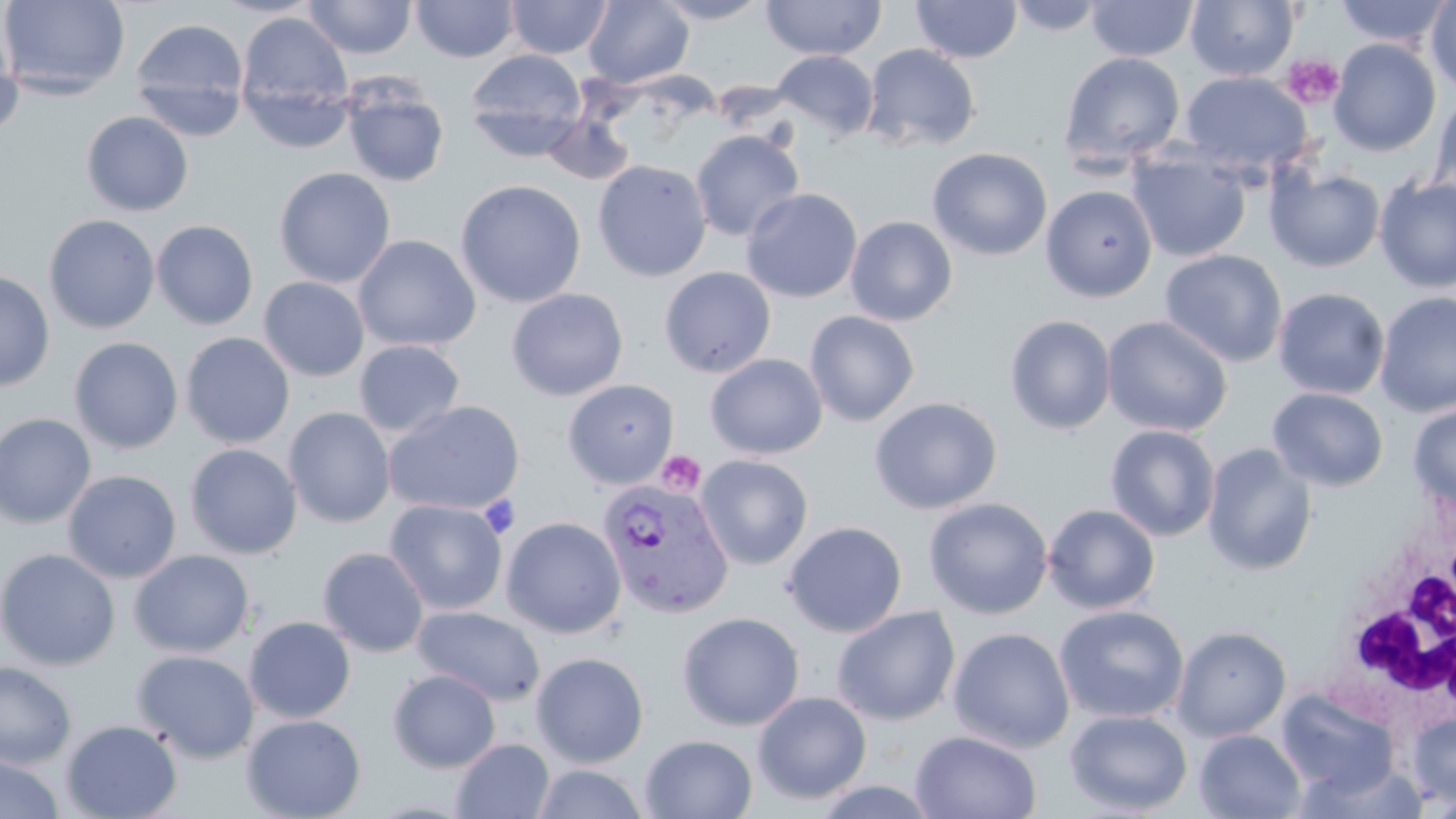
slide_level_diagnosis: Plasmodium vivax
white_blood_cell_locations: 'approximate bounding boxes as (x1,y1)-(x2,y2) corner pairs in pixels: (1334,503)-(1455,720)'
modality: light microscopy
plasmodium_vivax_infected_red_blood_cell_locations: 'approximate bounding boxes as (x1,y1)-(x2,y2) corner pairs in pixels: (597,478)-(734,618)'
image_size: 1456×819 pixels
platelet_locations: 'approximate bounding boxes as (x1,y1)-(x2,y2) corner pairs in pixels: (1282,54)-(1344,109), (656,450)-(705,496), (478,494)-(520,538)'
uninfected_red_blood_cell_locations: 'approximate bounding boxes as (x1,y1)-(x2,y2) corner pairs in pixels: (0,0)-(130,99), (303,0)-(417,59), (411,0)-(520,62), (506,0)-(612,59), (651,0)-(770,24), (760,0)-(887,60), (1005,0)-(1107,35), (1185,0)-(1299,81), (1425,0)-(1456,94), (583,1)-(694,89), (910,1)-(1023,63), (1085,1)-(1199,61), (1334,1)-(1453,48), (237,11)-(354,137), (1,18)-(25,140), (129,18)-(250,136), (1329,39)-(1441,156), (862,43)-(980,153), (465,48)-(587,159), (771,49)-(879,141), (1058,51)-(1186,173), (1178,72)-(1313,179), (341,79)-(449,188), (1430,89)-(1456,206), (82,111)-(194,216), (539,112)-(636,186), (690,129)-(805,241), (1127,146)-(1251,262), (927,147)-(1052,261), (592,159)-(712,282), (1266,164)-(1385,273), (274,167)-(395,288), (1373,174)-(1456,293), (455,179)-(586,308), (1041,184)-(1158,302), (741,188)-(863,303), (43,214)-(160,334), (845,216)-(957,326), (152,220)-(258,330), (353,234)-(481,352), (1159,249)-(1287,368), (659,266)-(776,378), (0,269)-(55,391), (258,277)-(369,381), (1272,287)-(1391,400), (505,288)-(628,401), (1375,291)-(1456,417), (804,310)-(920,427), (1004,314)-(1117,435), (1101,315)-(1233,437), (181,332)-(295,448), (68,337)-(183,454), (354,339)-(466,438), (705,353)-(828,459), (562,379)-(680,489), (1267,387)-(1388,492), (869,396)-(1002,515), (383,400)-(525,516), (1407,402)-(1456,512), (283,407)-(396,527), (0,413)-(96,527), (1105,424)-(1221,542), (185,443)-(302,559), (1202,443)-(1318,576), (695,454)-(814,570), (62,470)-(182,583), (923,497)-(1053,619), (384,498)-(507,614), (1043,503)-(1161,614), (501,516)-(627,638), (782,520)-(908,638), (317,546)-(430,657), (0,548)-(120,670), (129,549)-(254,657), (1053,605)-(1189,724), (412,606)-(545,705), (832,606)-(960,726), (677,611)-(805,730), (244,616)-(356,723), (1172,625)-(1292,741), (948,627)-(1075,753), (131,649)-(260,763), (531,651)-(649,768), (0,661)-(77,770), (388,668)-(501,772), (1277,688)-(1401,797), (752,691)-(872,804), (1064,709)-(1192,816), (242,714)-(366,819), (1406,714)-(1456,804), (61,719)-(182,819), (1194,729)-(1306,818), (910,730)-(1041,818), (640,734)-(757,818), (451,737)-(554,819), (0,755)-(64,819), (532,764)-(649,819)'
preparation: thin blood smear
stain: May-Grünwald-Giemsa
magnification: 1000x
field_of_view: one of a larger specimen